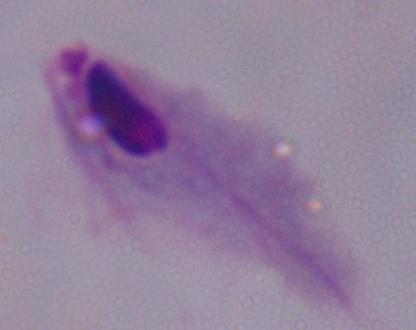

magnification = 1000x
identification = trichomonad
modality = photomicrograph